Find the cells and give the type of each one.
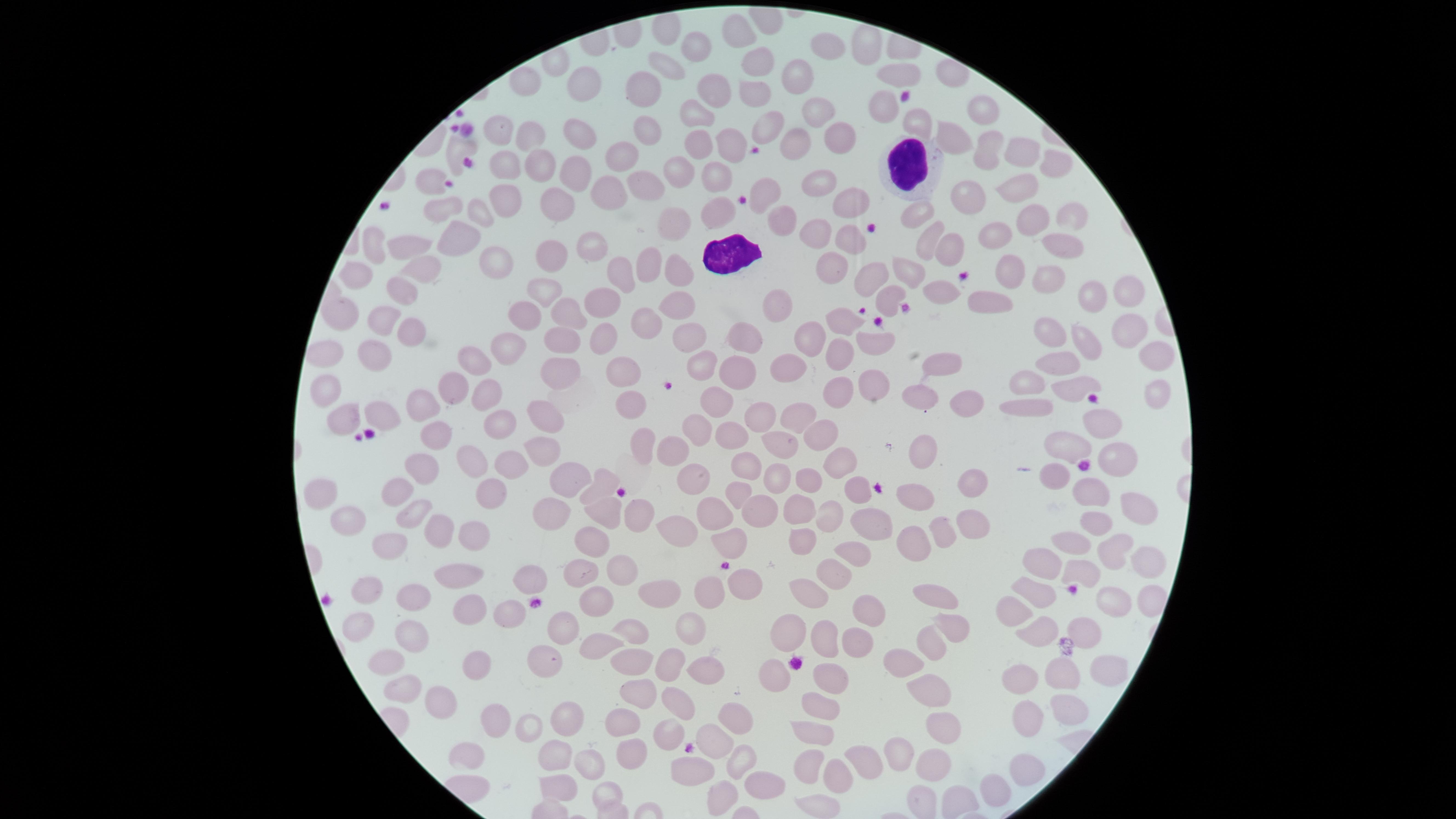

No parasitized red blood cells identified.
Approximate marker points, in pixels from the top-left corner.
Uninfected red blood cells: (x=666, y=32), (x=739, y=37), (x=868, y=44), (x=701, y=46), (x=824, y=47), (x=669, y=65), (x=749, y=66), (x=899, y=75), (x=793, y=77), (x=588, y=82), (x=638, y=85), (x=717, y=93), (x=749, y=96), (x=875, y=99), (x=812, y=110), (x=980, y=110), (x=694, y=118), (x=645, y=125), (x=917, y=125), (x=501, y=128), (x=763, y=128), (x=527, y=129), (x=581, y=136), (x=952, y=136), (x=836, y=137), (x=793, y=140), (x=727, y=145), (x=456, y=150), (x=1023, y=150), (x=620, y=152), (x=989, y=152), (x=699, y=154), (x=1055, y=160), (x=502, y=161), (x=574, y=163), (x=534, y=168), (x=811, y=177), (x=718, y=178), (x=679, y=181), (x=430, y=182), (x=1021, y=183), (x=641, y=189), (x=602, y=190), (x=766, y=194), (x=500, y=195), (x=968, y=195), (x=844, y=197), (x=552, y=207), (x=718, y=207), (x=448, y=211), (x=484, y=211), (x=918, y=217), (x=1029, y=217), (x=1068, y=217), (x=781, y=222), (x=673, y=225), (x=996, y=233), (x=847, y=235), (x=818, y=236), (x=931, y=241), (x=404, y=244), (x=593, y=244), (x=1050, y=244), (x=456, y=245), (x=948, y=246), (x=371, y=249), (x=557, y=257), (x=495, y=261), (x=833, y=265), (x=415, y=266), (x=647, y=267), (x=620, y=271), (x=906, y=271), (x=1010, y=271), (x=673, y=273), (x=351, y=274), (x=1044, y=274), (x=872, y=276), (x=1125, y=289), (x=399, y=291), (x=545, y=292), (x=944, y=293), (x=1088, y=296), (x=673, y=300), (x=884, y=300), (x=596, y=306), (x=985, y=306), (x=779, y=309), (x=341, y=314), (x=560, y=314), (x=847, y=322), (x=376, y=323), (x=650, y=324), (x=519, y=325), (x=407, y=330), (x=1047, y=331), (x=1121, y=331), (x=746, y=332), (x=598, y=336), (x=682, y=340), (x=812, y=340), (x=1089, y=340), (x=867, y=341), (x=559, y=343), (x=324, y=347), (x=502, y=348), (x=373, y=355), (x=840, y=355), (x=1157, y=355), (x=473, y=357), (x=938, y=364), (x=786, y=368), (x=1072, y=368), (x=738, y=370), (x=558, y=371), (x=704, y=371), (x=620, y=375), (x=1028, y=380), (x=873, y=384), (x=1071, y=384), (x=1156, y=387), (x=454, y=389), (x=834, y=392), (x=721, y=394), (x=922, y=394), (x=487, y=395), (x=965, y=395), (x=1028, y=400), (x=423, y=407), (x=628, y=408), (x=547, y=410), (x=794, y=412), (x=350, y=413), (x=384, y=413), (x=1092, y=413), (x=761, y=420), (x=699, y=426), (x=503, y=429), (x=811, y=432), (x=431, y=436), (x=735, y=436), (x=641, y=443), (x=1064, y=445), (x=1114, y=446), (x=681, y=447), (x=541, y=448), (x=918, y=448), (x=781, y=449), (x=834, y=456), (x=746, y=460), (x=477, y=462), (x=512, y=464), (x=426, y=472), (x=1063, y=473), (x=777, y=474), (x=806, y=474), (x=574, y=478), (x=972, y=478), (x=693, y=480), (x=856, y=485), (x=393, y=487), (x=598, y=487), (x=1097, y=490), (x=323, y=492), (x=736, y=493), (x=491, y=494), (x=912, y=495), (x=796, y=505), (x=1138, y=508), (x=754, y=509), (x=403, y=511), (x=600, y=511), (x=822, y=512), (x=635, y=514), (x=706, y=514), (x=555, y=515), (x=967, y=519), (x=347, y=520), (x=1090, y=521), (x=863, y=524), (x=426, y=527), (x=940, y=527), (x=679, y=529), (x=463, y=533), (x=591, y=538), (x=1070, y=538), (x=725, y=539), (x=793, y=541), (x=402, y=544), (x=1106, y=546), (x=904, y=548), (x=852, y=551), (x=1048, y=563), (x=1138, y=563), (x=613, y=567), (x=1079, y=568), (x=459, y=571), (x=831, y=575), (x=582, y=576), (x=739, y=579), (x=532, y=583), (x=361, y=588), (x=942, y=589), (x=668, y=591), (x=807, y=591), (x=1033, y=594), (x=411, y=595), (x=704, y=595), (x=592, y=600), (x=1144, y=601), (x=1109, y=602), (x=462, y=607), (x=1009, y=608), (x=511, y=610), (x=873, y=617), (x=358, y=621), (x=692, y=624), (x=561, y=627), (x=632, y=627), (x=420, y=628), (x=953, y=632), (x=1081, y=632), (x=790, y=633), (x=1031, y=633), (x=823, y=640), (x=855, y=641), (x=605, y=642), (x=928, y=650), (x=544, y=656), (x=631, y=660), (x=901, y=661), (x=385, y=665), (x=474, y=668), (x=664, y=669), (x=701, y=673), (x=1019, y=673), (x=1097, y=673), (x=822, y=674), (x=769, y=675), (x=1058, y=675), (x=398, y=689), (x=937, y=691), (x=634, y=697), (x=438, y=701), (x=1059, y=701), (x=676, y=702), (x=820, y=702), (x=733, y=715), (x=1024, y=717), (x=505, y=718), (x=563, y=719), (x=628, y=720), (x=534, y=724), (x=671, y=730), (x=813, y=731), (x=944, y=734), (x=711, y=743), (x=554, y=753), (x=627, y=753), (x=899, y=753), (x=469, y=755), (x=870, y=759), (x=738, y=761), (x=807, y=761), (x=594, y=764), (x=687, y=765), (x=934, y=765), (x=1021, y=767), (x=836, y=775), (x=994, y=783), (x=765, y=785), (x=720, y=787), (x=602, y=789), (x=555, y=790), (x=920, y=796), (x=957, y=798), (x=816, y=809).
White blood cells: (x=903, y=157), (x=731, y=250).

stain = Giemsa
preparation = thin blood film
field of view = single
image size = 1456×819 pixels
capture = smartphone photograph through the microscope eyepiece
visible region = circular